Report the malaria status of this cell.
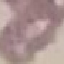

It is uninfected.

image type = automatically extracted cell patch, resized to 64 × 64 pixels
stain = Giemsa
capture = smartphone camera at the microscope eyepiece
preparation = thin blood smear